Assess this cell for malaria.
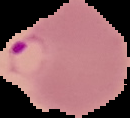
Parasitized.

image size = 130×118 pixels
image type = segmented cell region with the area outside set to black
preparation = thin blood smear